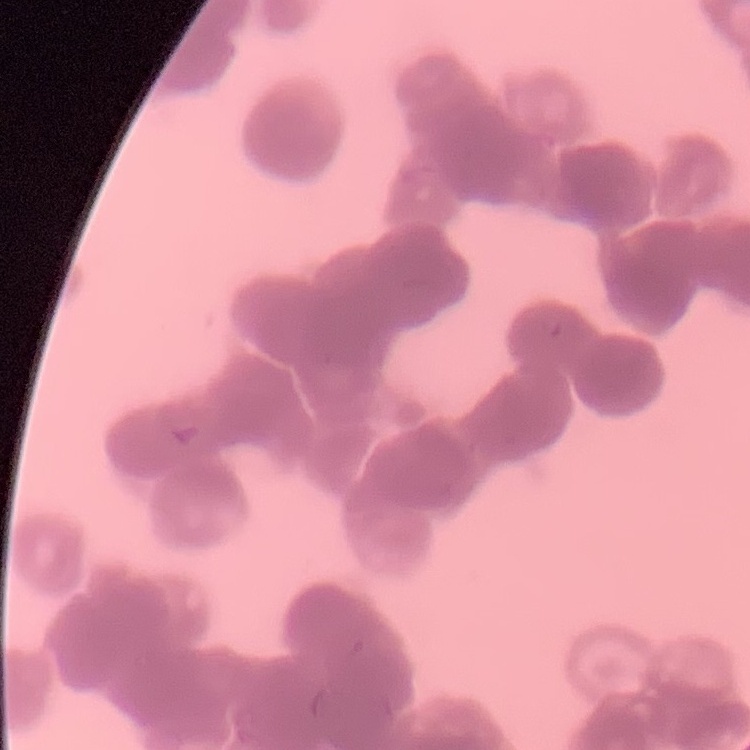

red blood cell morphology = rouleaux formation
image type = square crop of a larger photomicrograph
preparation = thin peripheral smear
stain = Field's or Giemsa